Assess this cell for malaria.
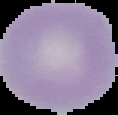
It is uninfected.

Summary:
  - Image size: 118×115 pixels
  - Image type: segmented cell region on a black background
  - Preparation: thin blood film